Give the extent of all uninfected red blood cells.
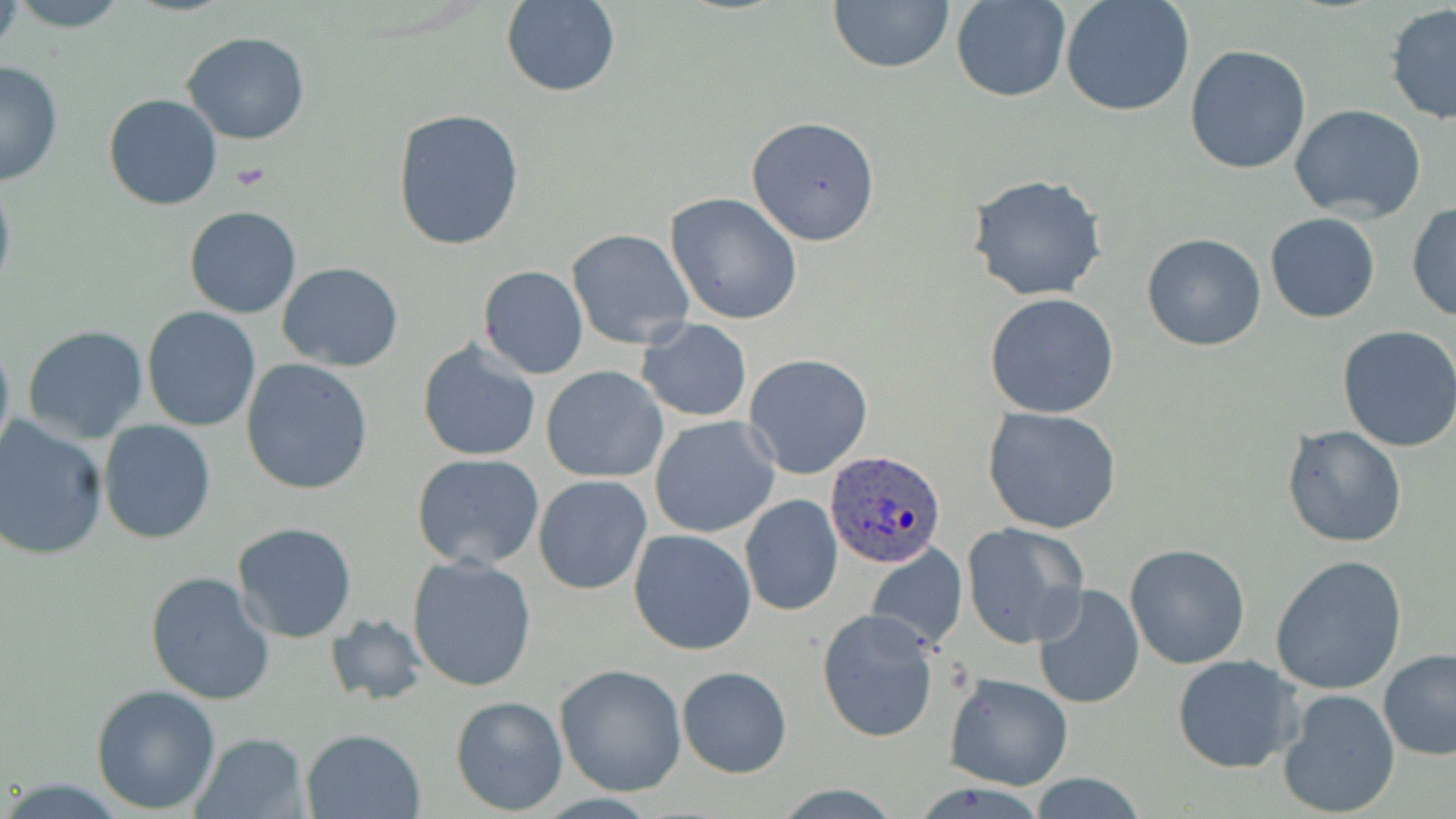

Approximate bounding boxes as [x1, y1, x2, y2] in pixels.
Uninfected red blood cells: [8, 0, 133, 31], [829, 0, 955, 72], [951, 0, 1071, 103], [1060, 0, 1195, 117], [502, 2, 619, 98], [1384, 5, 1456, 127], [181, 31, 311, 145], [1184, 44, 1312, 174], [0, 61, 64, 187], [102, 94, 223, 211], [1290, 104, 1427, 223], [392, 107, 527, 254], [745, 116, 881, 245], [0, 171, 16, 307], [968, 173, 1110, 303], [664, 192, 804, 325], [1406, 201, 1456, 324], [183, 205, 301, 318], [1265, 211, 1380, 323], [567, 228, 695, 349], [1142, 234, 1267, 351], [278, 264, 403, 370], [477, 265, 589, 379], [984, 293, 1119, 419], [141, 306, 264, 432], [639, 319, 752, 422], [21, 325, 149, 444], [1337, 326, 1456, 451], [0, 328, 15, 464], [417, 340, 542, 463], [743, 353, 874, 479], [240, 359, 373, 495], [541, 366, 669, 484], [982, 405, 1124, 536], [0, 416, 108, 561], [649, 416, 781, 539], [97, 420, 217, 544], [1281, 424, 1408, 549], [410, 452, 546, 570], [533, 476, 652, 594], [739, 494, 844, 618], [961, 522, 1089, 649], [231, 523, 359, 645], [628, 527, 755, 656], [866, 543, 967, 653], [1125, 543, 1252, 669], [406, 554, 538, 692], [1271, 555, 1407, 695], [143, 572, 276, 705], [1031, 585, 1144, 709], [816, 608, 940, 743], [325, 614, 430, 706], [1378, 650, 1456, 760], [1172, 654, 1298, 774], [555, 664, 688, 797], [677, 667, 792, 777], [943, 673, 1074, 790], [90, 684, 221, 813], [1276, 688, 1402, 815], [450, 695, 568, 816], [299, 727, 426, 819], [189, 733, 309, 819], [1028, 774, 1146, 818].

Plasmodium ovale-infected red blood cell locations: [826, 450, 946, 570]. Platelet locations: [233, 162, 271, 191]. Slide-level diagnosis: Plasmodium ovale. Light microscopy. May-Grünwald-Giemsa stain. Thin blood film. One field of a larger specimen. Image is 1456×819 pixels. Captured at 1000x magnification.